Report the malaria status of this cell.
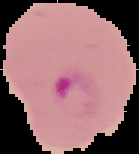

It is parasitized.

image size = 139×154 pixels
preparation = thin blood film
image type = segmented cell region on a black background